Assess this cell for malaria.
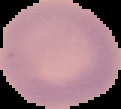

Uninfected.

From a thin blood smear. Image is 121×109 pixels. Segmented cell region on a black background.